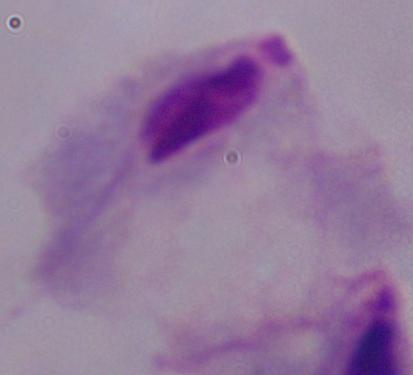 A trichomonad is shown. Micrograph. Captured at 1000x magnification.